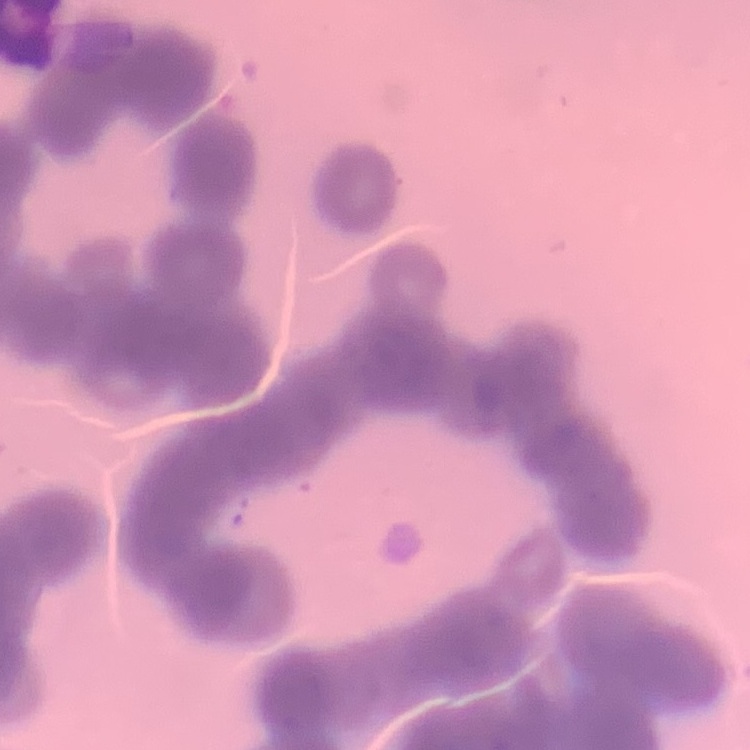
The erythrocytes show rouleaux formation. Field's or Giemsa stain. One tile cut from a larger photomicrograph. Thin blood smear.